Describe the morphology of the red blood cells.
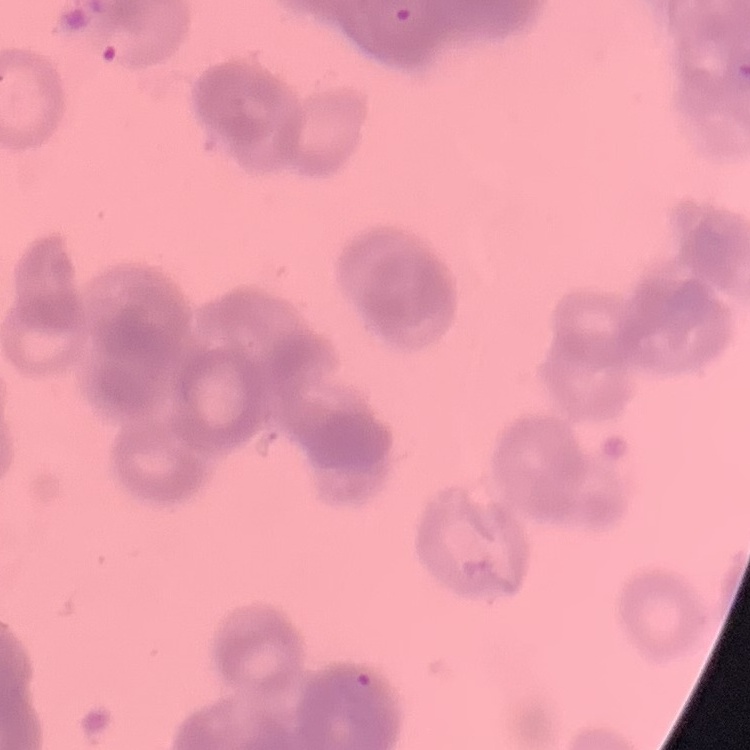
Rouleaux formation.

Square crop of a larger photomicrograph. Stained with either Field's or Giemsa. Thin blood film.